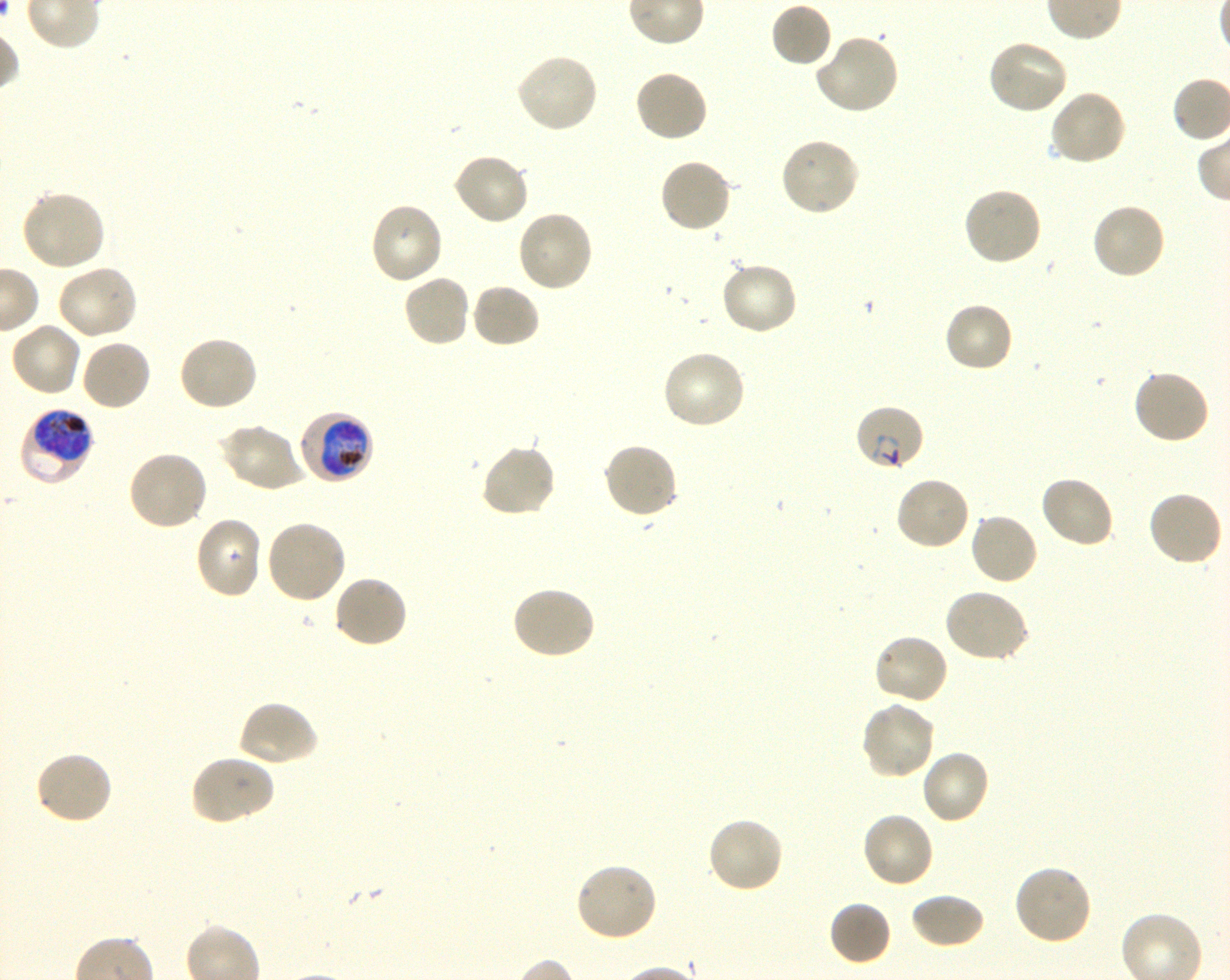

Approximate bounding boxes as {x1, y1, x2, y2} in pixels. Not every red blood cell is marked. A life-cycle stage — or a range of stages, where the recorded stages span more than one — follows each staged infected red blood cell.
Summary:
  - Locations of infected red blood cells: {853, 402, 925, 472} ring; {19, 406, 96, 487} late trophozoite to early schizont; {296, 410, 375, 485} trophozoite
  - Locations of uninfected red blood cells: {770, 3, 832, 68}, {814, 31, 900, 115}, {986, 38, 1070, 116}, {514, 51, 600, 134}, {633, 69, 709, 144}, {1049, 88, 1127, 167}, {778, 135, 861, 218}, {451, 152, 531, 227}, {658, 157, 733, 236}, {961, 186, 1044, 267}, {18, 188, 105, 272}, {368, 200, 444, 286}, {1090, 201, 1167, 280}, {515, 208, 594, 293}, {719, 261, 799, 337}, {55, 264, 139, 341}, {401, 273, 472, 348}, {472, 283, 541, 349}, {942, 301, 1014, 374}, {9, 321, 83, 397}, {177, 335, 260, 413}, {79, 338, 152, 413}, {661, 348, 748, 431}, {1132, 368, 1211, 446}, {219, 423, 308, 493}, {602, 441, 679, 520}, {479, 442, 557, 519}, {126, 450, 209, 532}, {1038, 474, 1116, 550}, {894, 475, 972, 552}, {1146, 490, 1224, 569}, {969, 511, 1040, 586}, {194, 515, 264, 600}, {264, 519, 347, 604}, {331, 574, 409, 650}, {510, 584, 596, 661}, {942, 587, 1030, 663}, {872, 633, 950, 706}, {237, 699, 319, 768}, {858, 699, 937, 781}, {919, 748, 992, 826}, {33, 750, 114, 826}, {189, 753, 275, 825}, {860, 811, 935, 889}, {706, 816, 785, 895}, {574, 862, 659, 943}, {1013, 863, 1094, 946}, {909, 891, 985, 950}, {828, 900, 892, 966}
  - Life-cycle stages observed: ring, trophozoite
  - Objective: 100x, oil immersion, numerical aperture 1.30
  - Donor blood group: O+
  - Stain: Giemsa
  - Image size: 1230×980 pixels
  - Preparation: thin blood film
  - Culture: in-vitro P. falciparum strain 3D7, shaking
  - Field of view: one from this slide